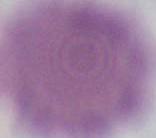

magnification: 1000x
modality: photomicrograph
identification: erythrocyte